Name the cell type shown.
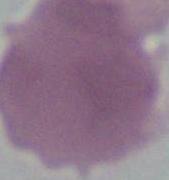

This is an erythrocyte.

Photomicrograph. Captured at 1000x magnification.